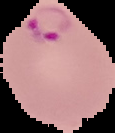
Image is 115×133 pixels. Segmented cell region on a black background. From a thin blood smear. Result: Plasmodium parasites identified.